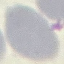
Result: negative for malaria parasites. Photographed with a smartphone camera at the microscope eyepiece. Automatically extracted cell patch, resized to 64 × 64 pixels. Thin smear of blood. Giemsa stain.